Describe the morphology of the erythrocytes.
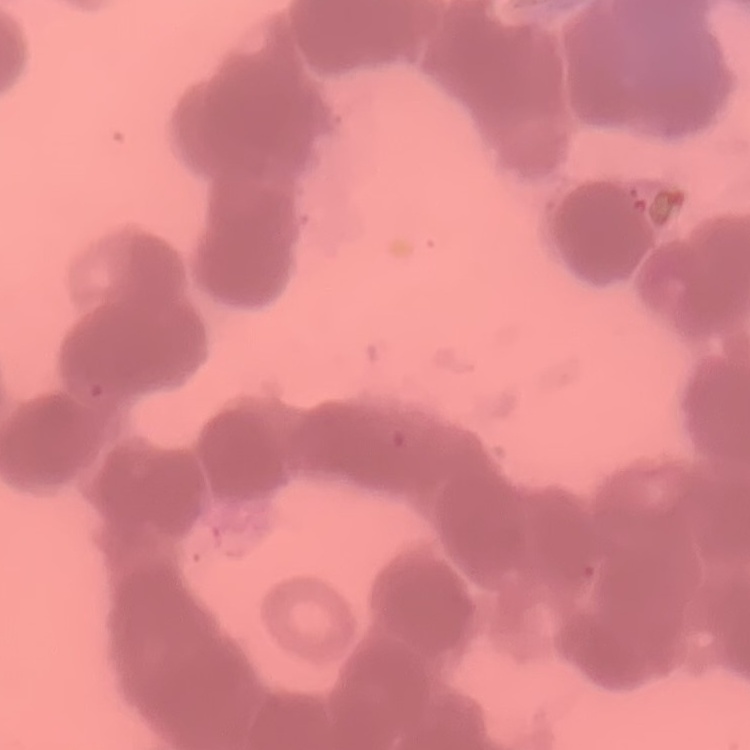
They show rouleaux formation.

stain = Field's or Giemsa
image type = square crop of a larger photomicrograph
preparation = thin peripheral smear